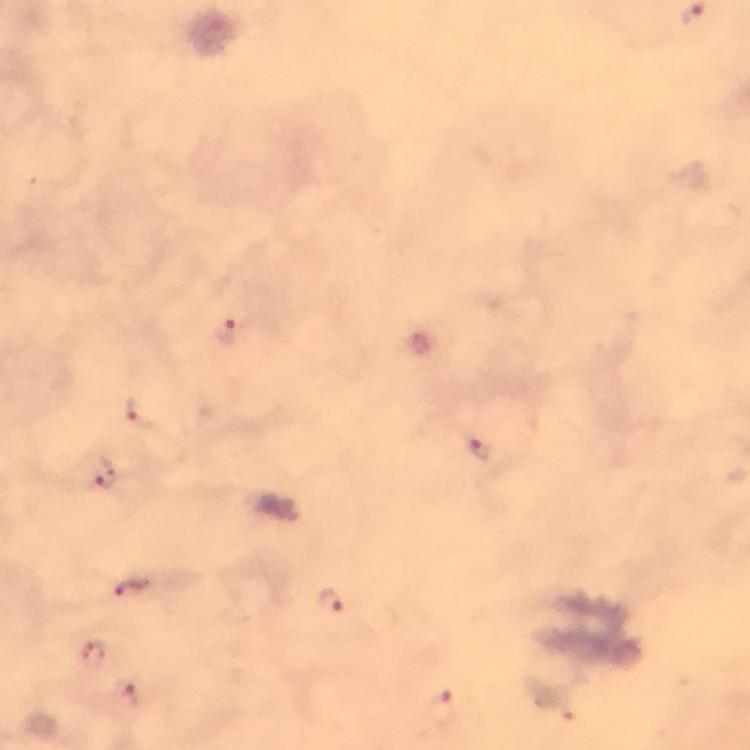

Approximate centers as [x, y] in pixels. Malaria parasite locations: [231, 332], [144, 414], [483, 450], [105, 474], [134, 587], [332, 602], [94, 652], [128, 695], [441, 707]. From a malaria diagnostic workup. Giemsa stain. At 100x magnification. Image is 750×750 pixels. Immersion oil was used. Thick blood smear. Cropped region of a single field of view. Smartphone photograph taken through a microscope.